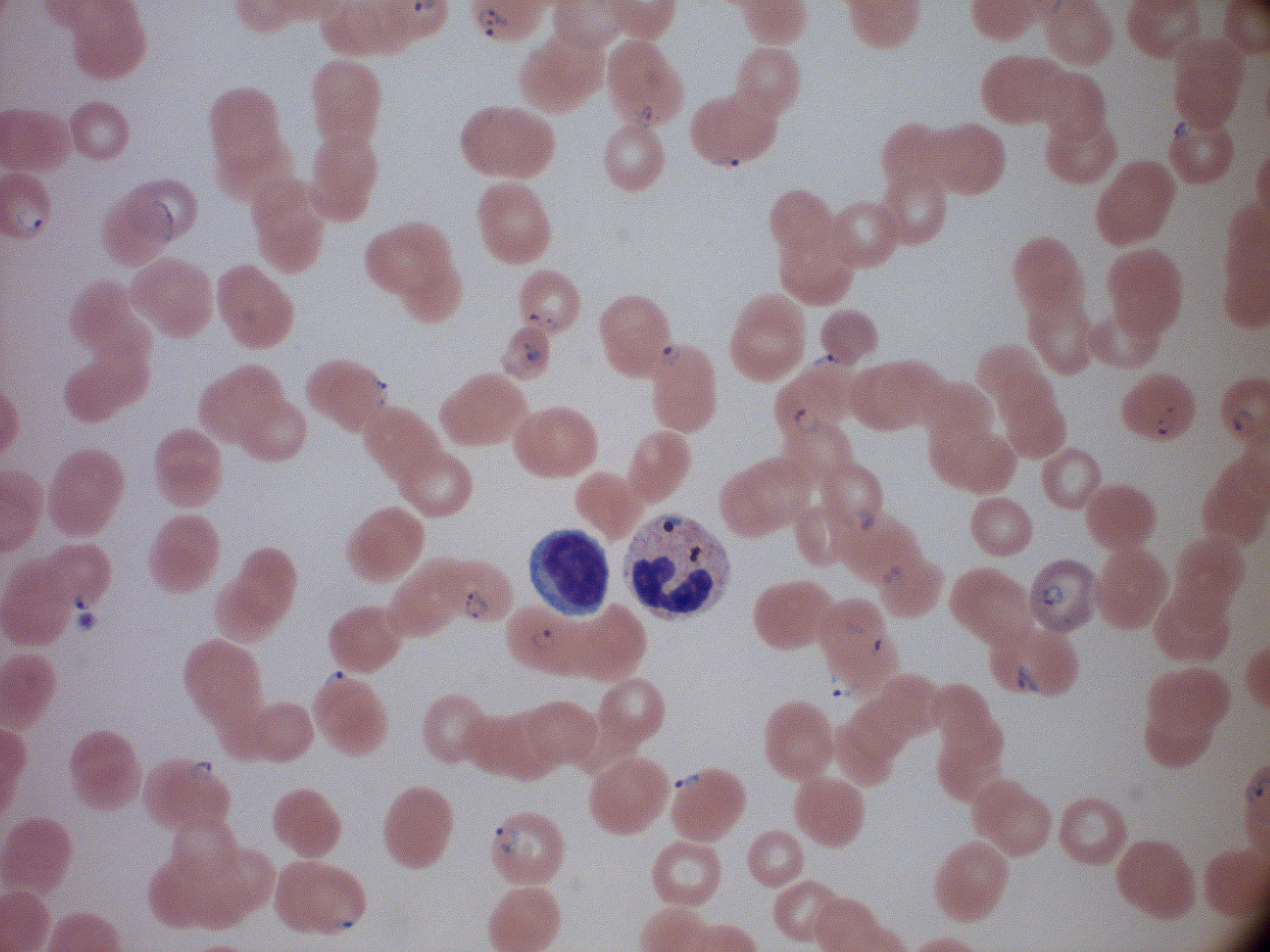 Approximate bounding boxes as [x1, y1, x2, y2] in pixels, from the source annotation, which is not necessarily exhaustive. Ring form locations: [474, 5, 514, 45], [629, 100, 662, 131], [1168, 115, 1203, 149], [707, 150, 746, 173], [8, 200, 46, 238], [525, 306, 563, 333], [519, 338, 545, 366], [651, 338, 684, 368], [806, 349, 846, 375], [364, 369, 391, 409], [791, 403, 823, 435], [1153, 404, 1182, 438], [1227, 404, 1259, 440], [841, 505, 879, 534], [877, 563, 906, 589], [1033, 576, 1067, 609], [69, 585, 99, 613], [461, 588, 492, 622], [524, 623, 562, 653], [870, 634, 891, 659], [1010, 661, 1047, 700], [318, 665, 354, 696], [826, 666, 862, 701], [184, 757, 216, 784], [669, 769, 703, 793], [491, 822, 525, 857], [331, 903, 361, 932]. Single field of view. Species: Plasmodium falciparum. Thin blood film. Giemsa stain. Acquired with a Leica DM2000 optical microscope and its built-in camera. Image is 1270×952 pixels. 100x magnification.